Assess the morphology of the erythrocytes.
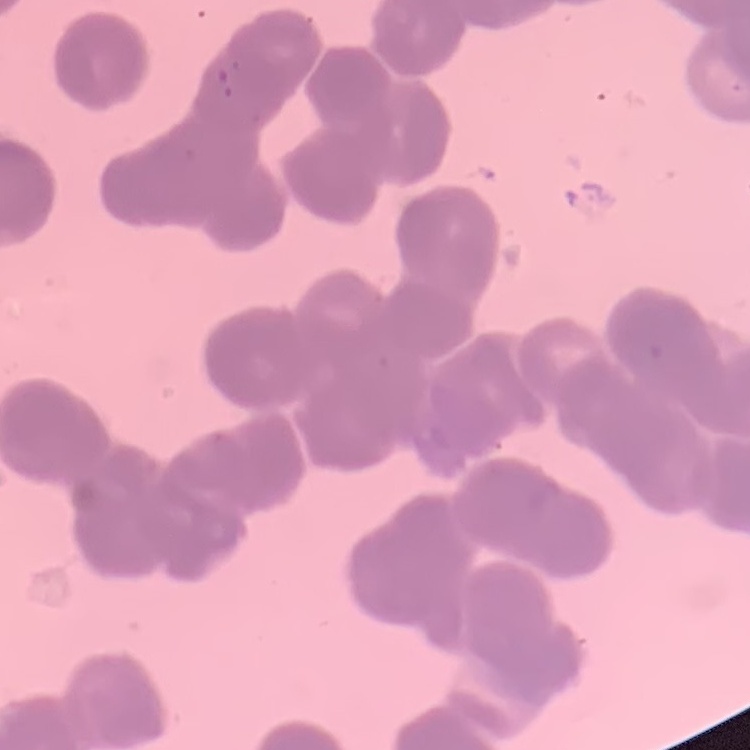

Rouleaux formation.

stain = Field's or Giemsa
image type = square crop of a larger photomicrograph
preparation = thin peripheral smear